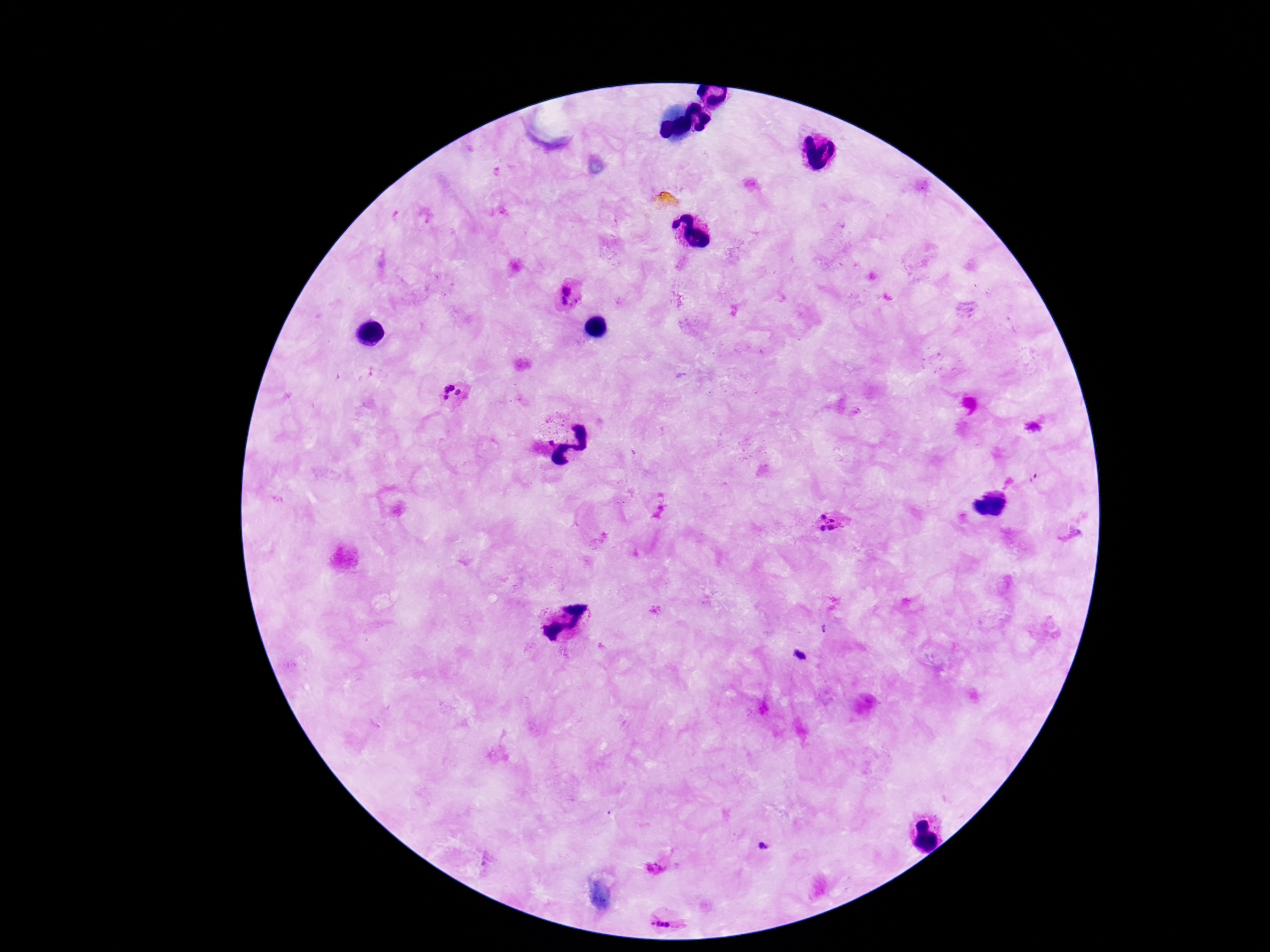
image size = 1270×952 pixels
preparation = thick blood smear
stain = Giemsa
Plasmodium parasite locations = approximate centers as [x, y] in pixels: [566, 291], [564, 301], [576, 301], [452, 388], [446, 390], [458, 393], [445, 398], [823, 517], [832, 520], [822, 528], [833, 528], [655, 866], [663, 921]
patient malaria status = infected
capture = smartphone camera through the microscope eyepiece
field of view = one from this slide
magnification = 100x